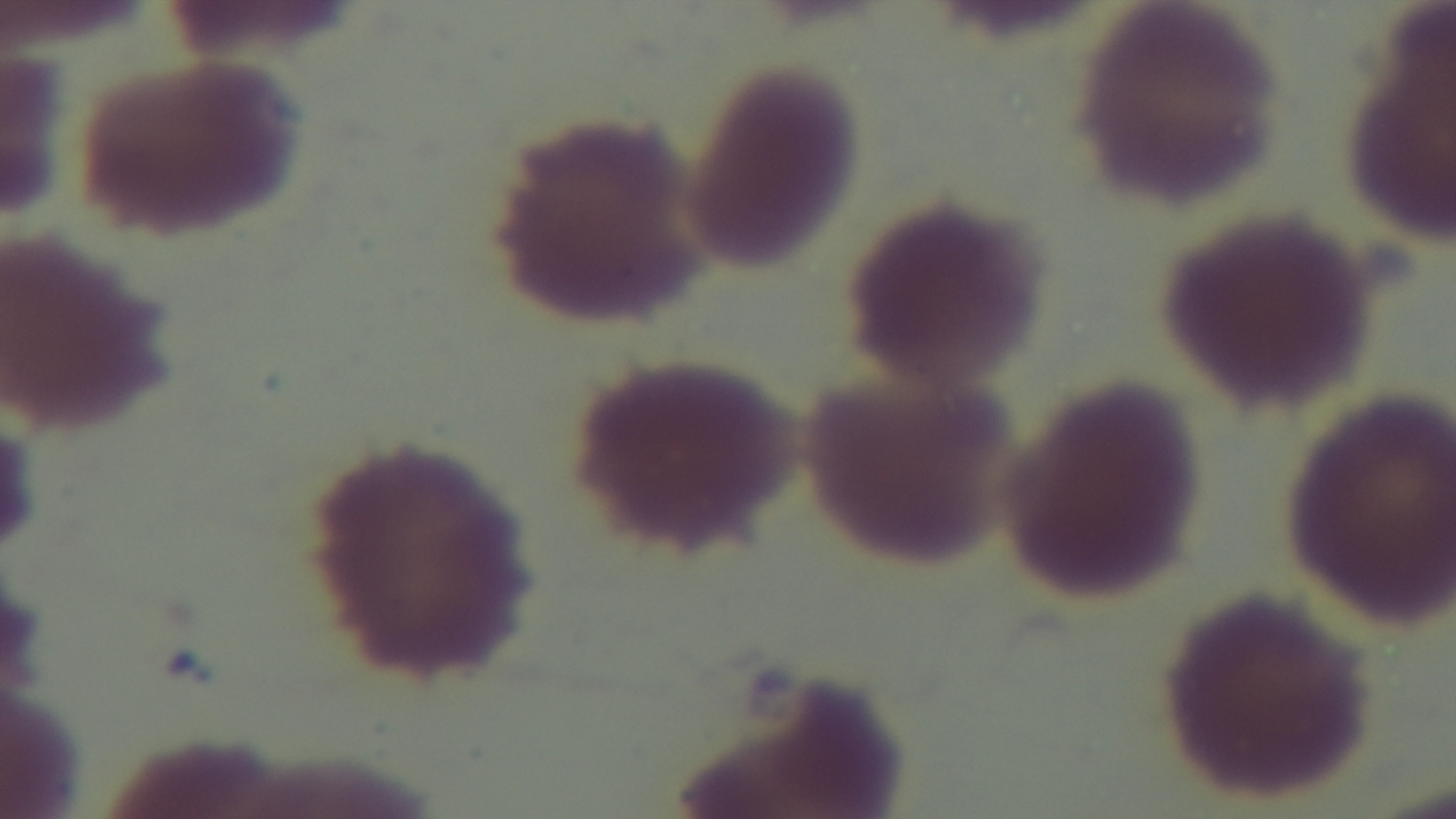
Single field of view. Preparation: thin smear. Light microscopy. Giemsa-stained. Oil-immersion objective, 100x. Malaria status: negative. Captured with a mounted 4K digital camera.